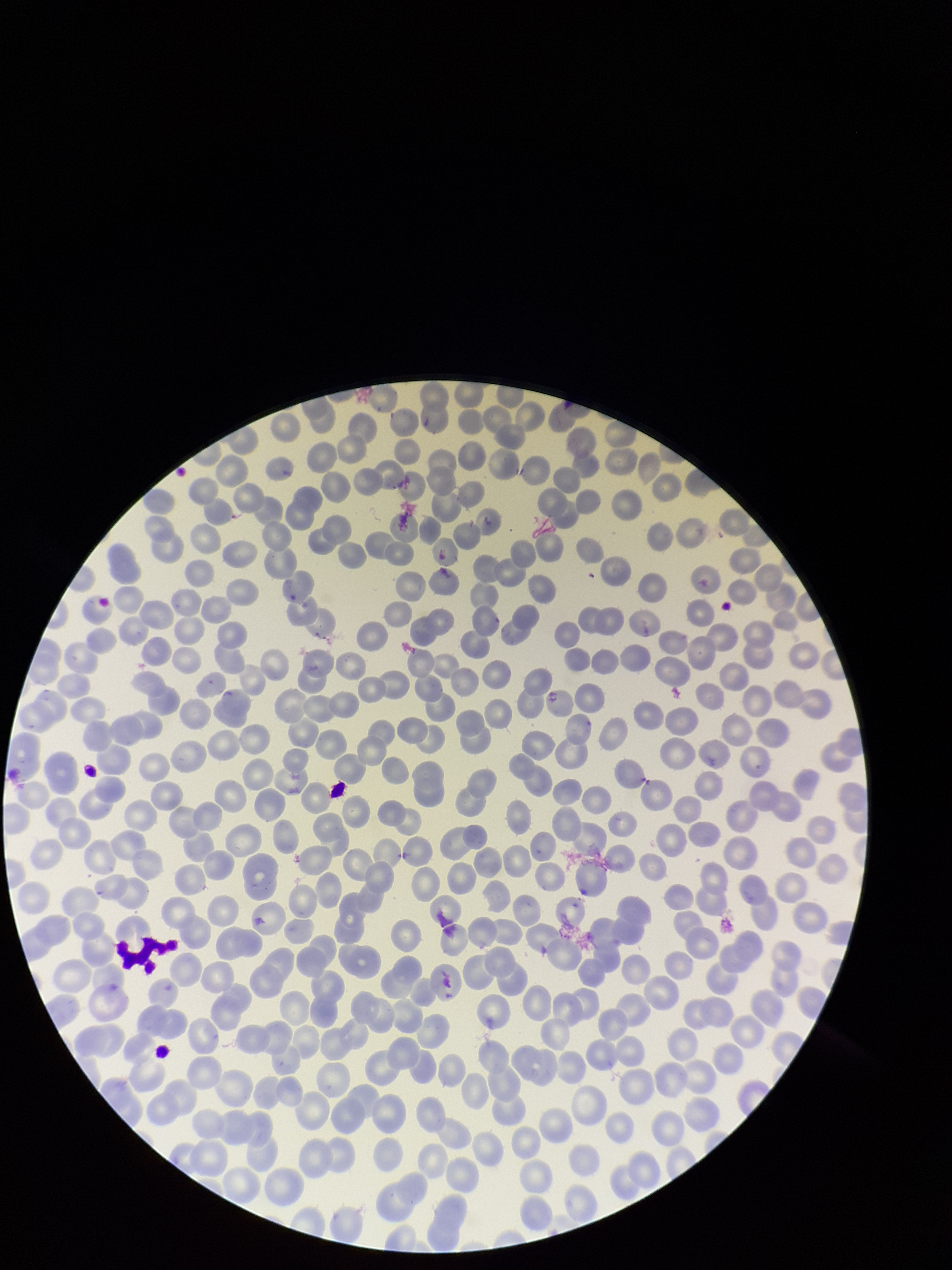

capture = smartphone photograph through the microscope eyepiece
parasitized red blood cell count = 0
species reported for this patient = Plasmodium vivax
red blood cell count = 237
patient malaria status = infected
image size = 952×1270 pixels
stain = Giemsa
parasitized red blood cells = none seen
preparation = thin
field of view = single